Classify this cell by malaria status.
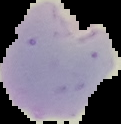
Parasitized.

image type = segmented cell region on a black background
preparation = thin blood film
image size = 121×124 pixels